Assess this cell for malaria.
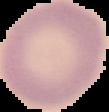

It is uninfected.

From a thin blood smear. Image is 109×112 pixels. The area outside the segmented cell region is set to black.